Report the malaria status of this cell.
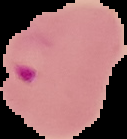

It is parasitized.

preparation: thin blood smear
image_size: 127×139 pixels
image_type: segmented cell region with the area outside set to black